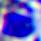

Photomicrograph. 400x magnification. A white blood cell is seen.